Point out every Plasmodium parasite and every leukocyte.
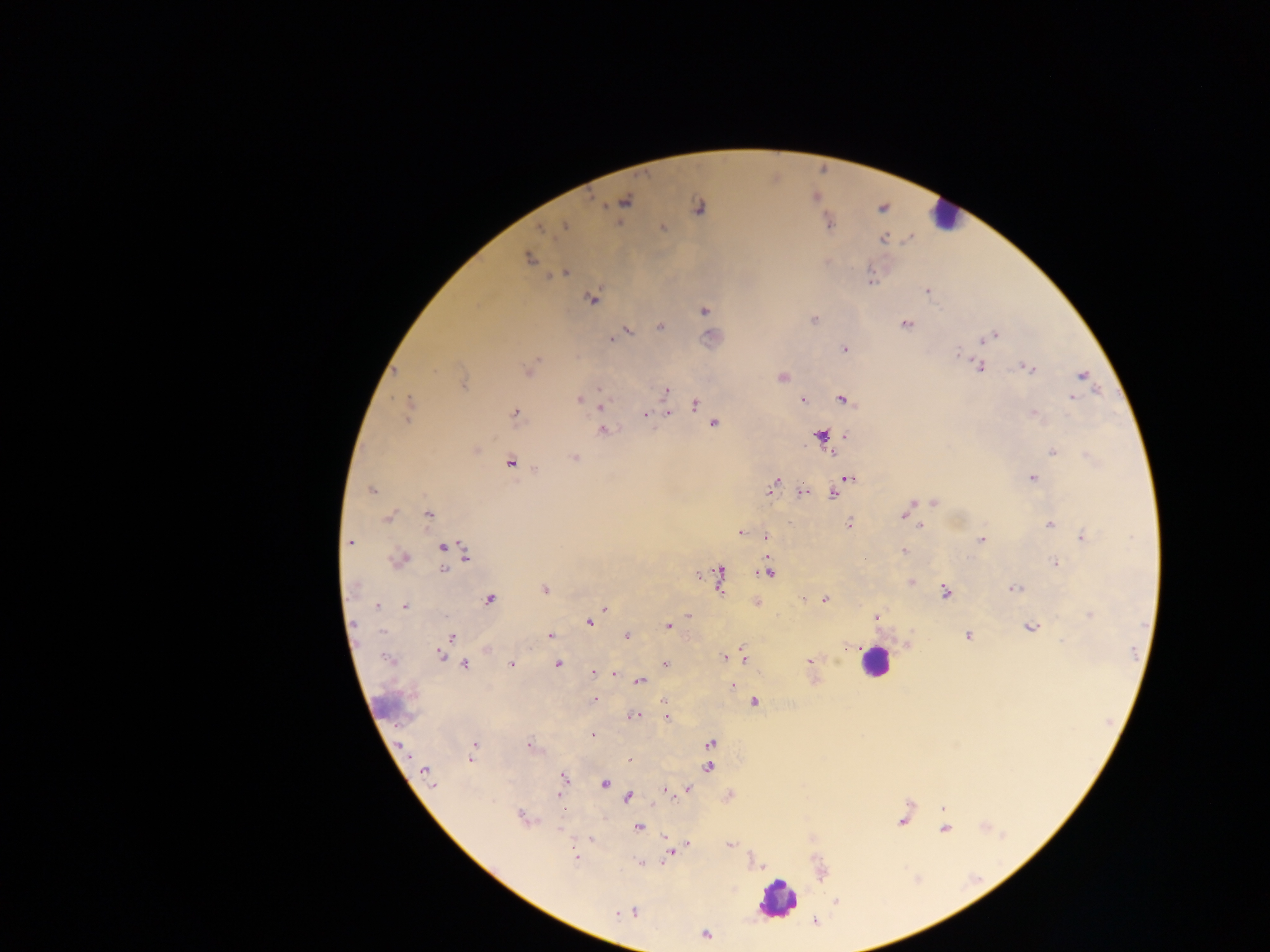
Approximate centers as x y in pixels.
Plasmodium parasites: 698 206; 566 226; 662 227; 542 229; 529 257; 567 273; 924 292; 590 298; 703 311; 814 320; 905 323; 659 327; 629 330; 995 334; 616 335; 612 337; 983 339; 844 349; 958 351; 1025 365; 981 368; 1031 368; 394 372; 1083 376; 782 378; 464 380; 600 388; 667 390; 1072 397; 578 400; 803 400; 841 400; 694 405; 409 407; 600 407; 514 412; 668 412; 1035 413; 645 416; 713 423; 605 431; 820 434; 478 448; 1052 452; 575 457; 512 463; 537 469; 850 479; 1033 479; 774 481; 371 488; 771 490; 801 491; 833 494; 933 502; 912 504; 430 513; 901 517; 385 518; 849 522; 1049 525; 922 526; 739 533; 1082 534; 766 535; 980 539; 351 543; 443 547; 902 551; 465 557; 1054 562; 442 567; 697 574; 769 574; 720 578; 545 589; 1014 589; 945 592; 825 598; 488 599; 803 599; 757 601; 377 606; 406 607; 606 608; 1088 614; 686 615; 876 616; 352 623; 590 623; 668 626; 1029 627; 626 635; 550 636; 966 636; 452 637; 845 647; 743 650; 441 655; 723 656; 743 658; 807 661; 464 663; 510 663; 664 663; 558 664; 592 673; 615 675; 640 682; 733 685; 594 700; 661 700; 754 701; 633 716; 667 719; 592 734; 528 741; 710 743; 400 745; 470 759; 629 759; 707 767; 423 771; 428 776; 563 778; 606 783; 433 784; 661 789; 688 789; 668 790; 560 797; 628 798; 655 805; 520 816; 557 828; 639 828; 591 838; 688 844; 729 844; 669 854; 638 864; 706 933.
Leukocytes: 945 211; 875 665; 777 899.

country = Ghana
field of view = single
capture = mobile-phone photograph through a microscope
image size = 1270×952 pixels
preparation = thick blood smear